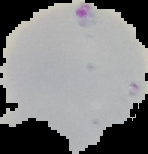 Malaria status: parasitized. Image is 148×154 pixels. The area outside the segmented cell region is set to black. From a thin blood smear.